Point out leukocytes.
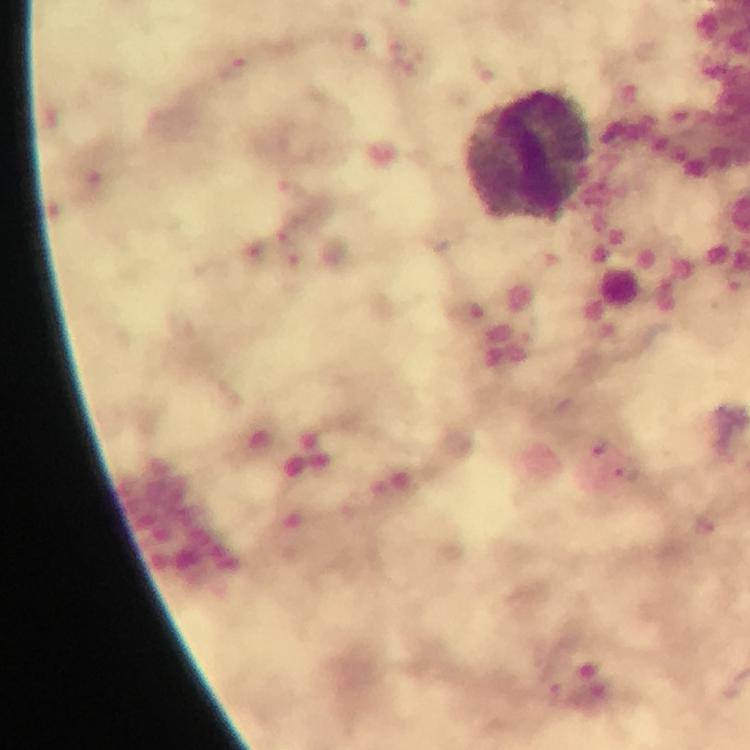
Approximate centers as [x, y] in pixels.
Leukocytes: [530, 157].

Summary:
  - Malaria parasite locations: [235, 68], [291, 189], [289, 249], [469, 314], [627, 471], [554, 692], [594, 698]
  - Cropped from: one field of view
  - Magnification: 100x
  - Immersion oil: used
  - Capture: smartphone photograph through a microscope
  - Context: from a malaria diagnostic workup
  - Preparation: thick blood smear
  - Stain: Giemsa
  - Image size: 750×750 pixels